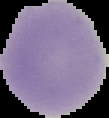

The area outside the segmented cell region is set to black. From a thin blood film. Malaria status: uninfected. Image is 109×118 pixels.